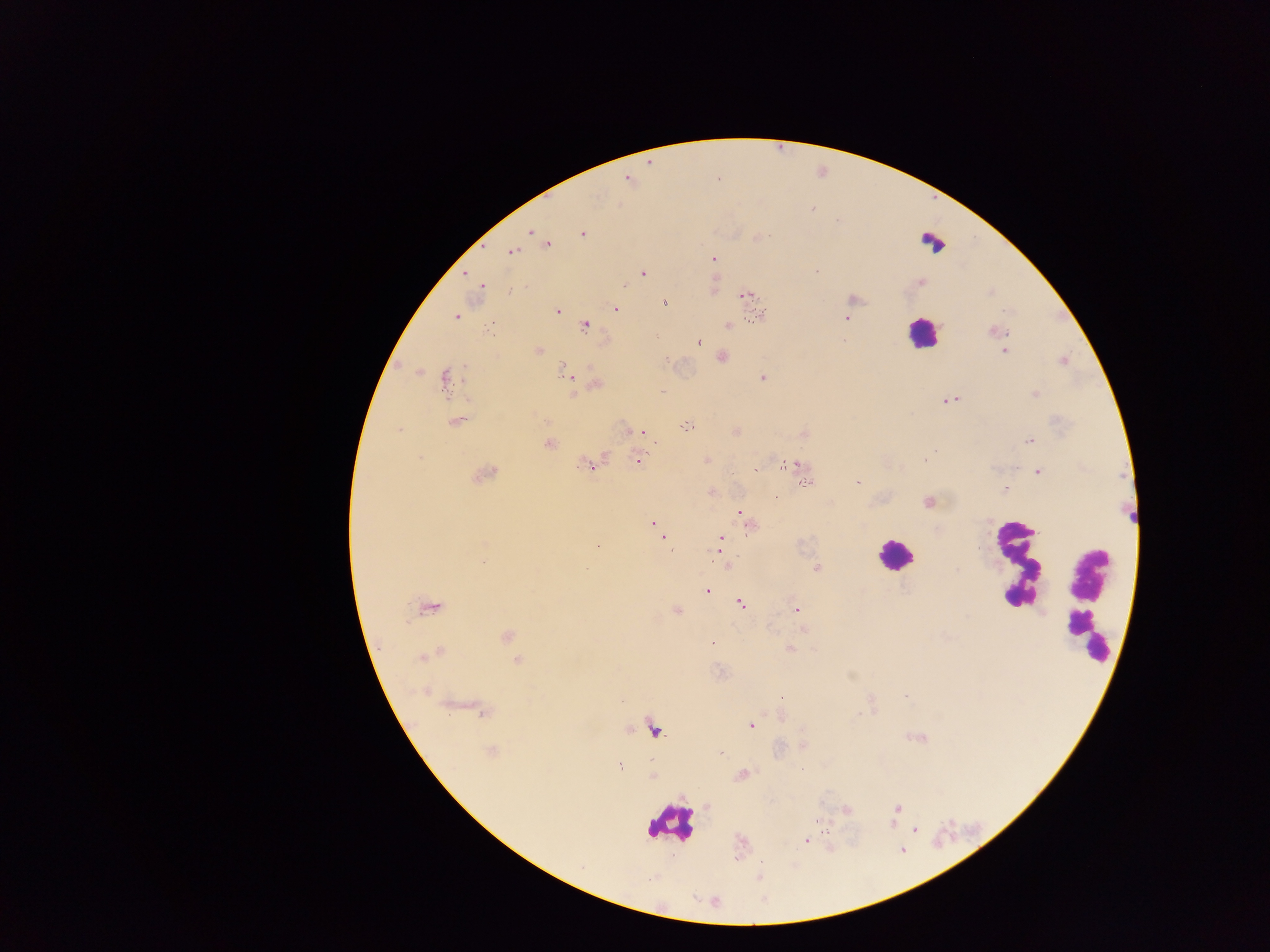

{
  "capture": "mobile-phone photograph through a microscope",
  "leukocyte_locations": "approximate centers as (x, y) in pixels: (931, 244), (921, 332), (894, 554), (1016, 562), (1087, 605), (672, 823)",
  "plasmodium_parasite_locations": "approximate centers as (x, y) in pixels: (811, 208), (530, 231), (583, 233), (542, 239), (547, 244), (511, 252), (713, 259), (642, 274), (624, 285), (481, 286), (747, 295), (664, 301), (616, 309), (557, 310), (457, 317), (757, 317), (845, 318), (728, 326), (586, 327), (996, 331), (656, 337), (699, 342), (538, 350), (1004, 351), (721, 357), (1064, 360), (565, 372), (763, 378), (445, 379), (597, 384), (662, 391), (1035, 394), (951, 400), (456, 421), (688, 426), (399, 429), (641, 433), (1029, 440), (549, 444), (638, 459), (925, 460), (587, 465), (787, 465), (801, 465), (756, 470), (1038, 472), (484, 475), (806, 482), (858, 483), (1004, 490), (776, 497), (928, 502), (742, 517), (655, 525), (750, 525), (660, 534), (720, 539), (720, 545), (597, 546), (726, 563), (816, 569), (707, 591), (741, 604), (430, 608), (677, 610), (795, 610), (803, 629), (507, 636), (713, 644), (789, 649), (429, 655), (518, 660), (483, 713), (751, 725), (654, 731), (804, 745), (492, 752), (721, 752), (620, 767), (742, 774), (897, 808), (846, 809), (915, 830), (807, 840)",
  "country": "Ghana",
  "field_of_view": "single",
  "image_size": "1270×952 pixels",
  "preparation": "thick blood smear"
}